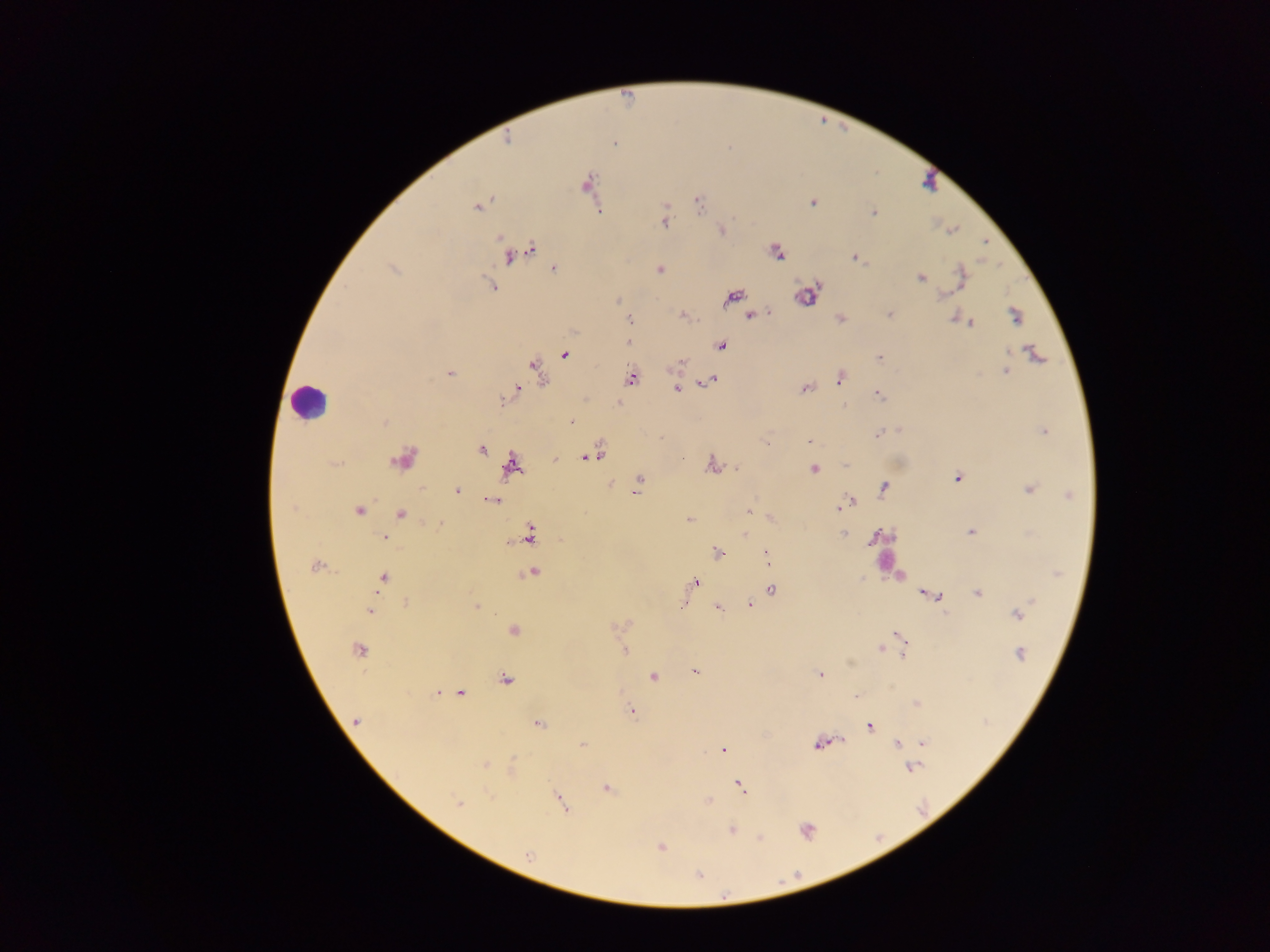

preparation: thick blood smear
field_of_view: single
leukocyte_locations: 'approximate centers as (x, y) in pixels: (307, 402), (885, 550)'
malaria_parasite_locations: 'approximate centers as (x, y) in pixels: (615, 143), (586, 184), (698, 202), (812, 203), (478, 207), (874, 212), (665, 222), (721, 230), (953, 230), (776, 252), (518, 254), (856, 258), (556, 268), (393, 269), (660, 270), (921, 278), (961, 279), (489, 285), (941, 295), (809, 296), (732, 297), (889, 315), (1015, 315), (753, 316), (840, 318), (955, 319), (630, 320), (970, 323), (629, 342), (721, 346), (1034, 354), (565, 355), (879, 358), (537, 370), (1005, 371), (449, 372), (631, 377), (840, 378), (710, 380), (677, 389), (805, 389), (516, 391), (879, 396), (503, 401), (572, 422), (1044, 431), (878, 433), (809, 442), (481, 449), (589, 457), (402, 460), (713, 465), (845, 465), (511, 466), (814, 468), (957, 478), (639, 480), (884, 487), (637, 489), (1029, 489), (457, 491), (1069, 495), (492, 500), (852, 500), (293, 507), (839, 508), (749, 509), (359, 511), (401, 514), (689, 520), (439, 524), (970, 532), (745, 533), (842, 533), (529, 534), (384, 538), (718, 553), (767, 557), (315, 566), (533, 572), (1058, 573), (383, 578), (696, 581), (772, 590), (978, 593), (932, 595), (942, 599), (406, 603), (750, 604), (682, 605), (476, 606), (718, 607), (370, 611), (1017, 614), (513, 630), (899, 636), (901, 643), (881, 648), (359, 649), (624, 651), (903, 652), (1020, 654), (850, 663), (696, 672), (821, 675), (653, 676), (505, 680), (438, 692), (460, 693), (856, 696), (916, 703), (632, 712), (357, 721), (539, 723), (870, 726), (841, 740), (827, 742), (923, 742), (818, 744), (897, 744), (583, 745), (723, 750), (485, 764), (914, 767), (740, 786), (606, 788), (559, 799), (708, 801), (458, 802), (731, 829), (806, 831), (760, 838), (661, 847), (528, 855), (698, 875), (725, 896)'
capture: mobile-phone photograph through a microscope
country: Ghana
image_size: 1270×952 pixels